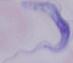
Summary:
  - Identification: trypanosome
  - Magnification: 1000x
  - Modality: micrograph